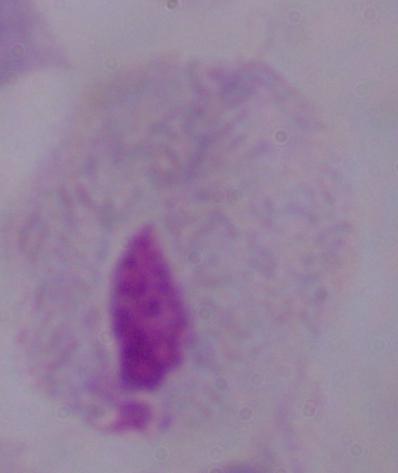
identification = trichomonad
magnification = 1000x
modality = photomicrograph